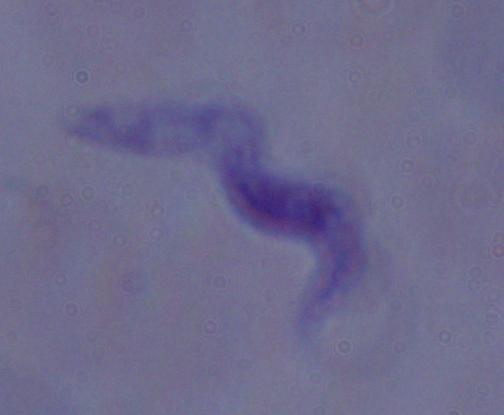
Summary:
  - Modality: photomicrograph
  - Magnification: 1000x
  - Identification: trypanosome